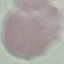
malaria status = uninfected
stain = Giemsa
preparation = thin smear
image type = cell patch, automatically extracted from a larger field of view and resized to 64 × 64 pixels
capture = smartphone camera at the microscope eyepiece